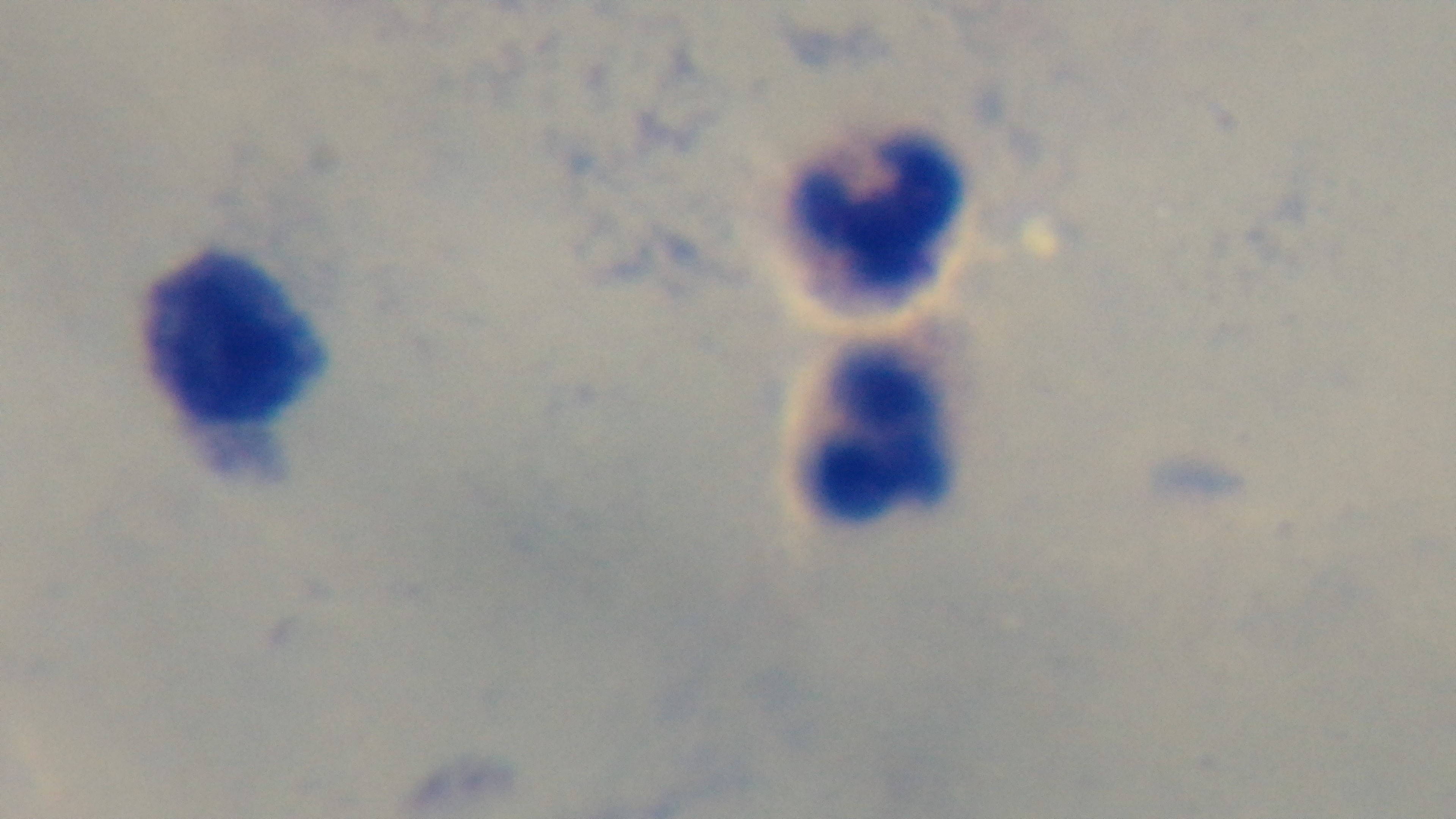

Summary:
  - Modality: light microscopy
  - Malaria status: uninfected
  - Capture: mounted 4K digital camera
  - Preparation: thick blood film
  - Field of view: single
  - Stain: Giemsa
  - Objective: 100x oil immersion